Assess this cell for malaria.
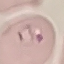

It is parasitized.

Automatically extracted cell patch, resized to 64 × 64 pixels. Giemsa-stained preparation. Thin blood smear. Photographed with a smartphone camera at the microscope eyepiece.